Report the malaria status of this cell.
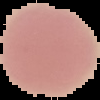
It is uninfected.

The area outside the segmented cell region is set to black. Image is 100×100 pixels. From a thin blood film.